Locate every malaria parasite.
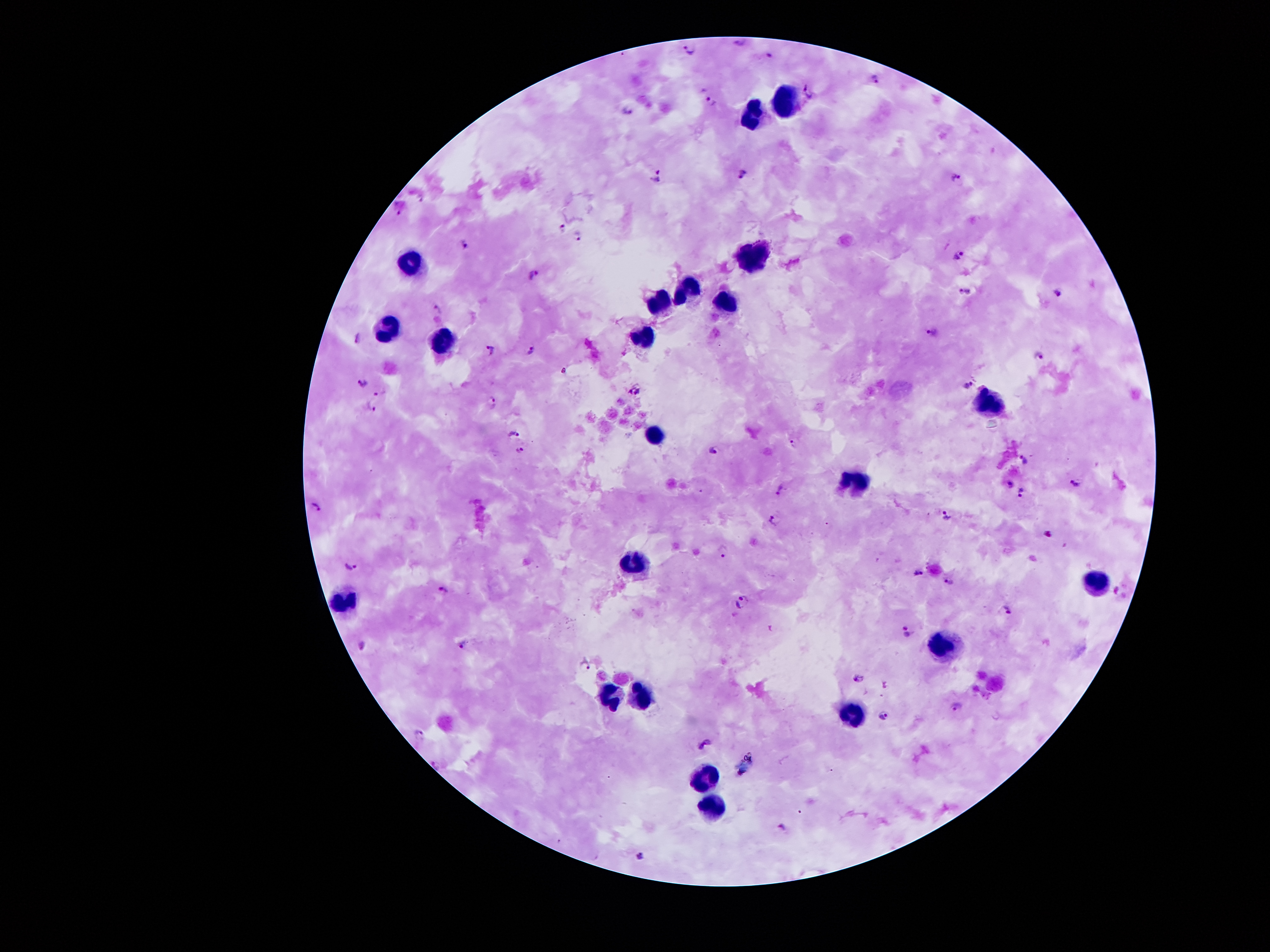
Approximate centers as {x, y} in pixels.
Malaria parasites: {740, 43}, {687, 48}, {769, 56}, {873, 79}, {806, 91}, {711, 100}, {629, 108}, {744, 174}, {660, 176}, {954, 177}, {421, 196}, {400, 211}, {561, 226}, {578, 236}, {465, 244}, {958, 254}, {532, 275}, {964, 292}, {1055, 292}, {436, 308}, {932, 333}, {357, 336}, {492, 349}, {530, 350}, {1038, 356}, {563, 369}, {364, 384}, {967, 386}, {630, 391}, {637, 391}, {380, 393}, {492, 402}, {371, 405}, {515, 433}, {795, 444}, {520, 449}, {713, 451}, {1024, 461}, {1077, 482}, {1010, 483}, {779, 490}, {1021, 492}, {315, 506}, {945, 515}, {773, 521}, {1048, 531}, {724, 551}, {351, 565}, {916, 570}, {948, 581}, {444, 588}, {742, 601}, {1007, 609}, {908, 631}, {464, 643}, {362, 644}, {586, 663}, {857, 677}, {957, 707}, {883, 714}, {420, 732}, {705, 743}, {436, 764}, {782, 826}, {640, 853}.

Leukocyte locations: {787, 99}, {751, 112}, {752, 255}, {410, 263}, {689, 287}, {727, 302}, {662, 303}, {391, 328}, {645, 337}, {444, 344}, {982, 402}, {654, 437}, {857, 481}, {635, 561}, {1092, 579}, {346, 598}, {939, 643}, {641, 697}, {611, 698}, {856, 715}, {706, 775}, {713, 809}. 100x magnification. Image is 1270×952 pixels. Giemsa-stained preparation. Thick peripheral-blood smear. Photographed through the microscope eyepiece with a smartphone camera. Patient malaria status: infected with Plasmodium falciparum. One field from this slide.